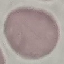 Result: negative for malaria parasites. Automatically extracted cell patch, resized to 64 × 64 pixels. Photographed with a smartphone camera at the microscope eyepiece. Giemsa-stained preparation. Thin smear of blood.